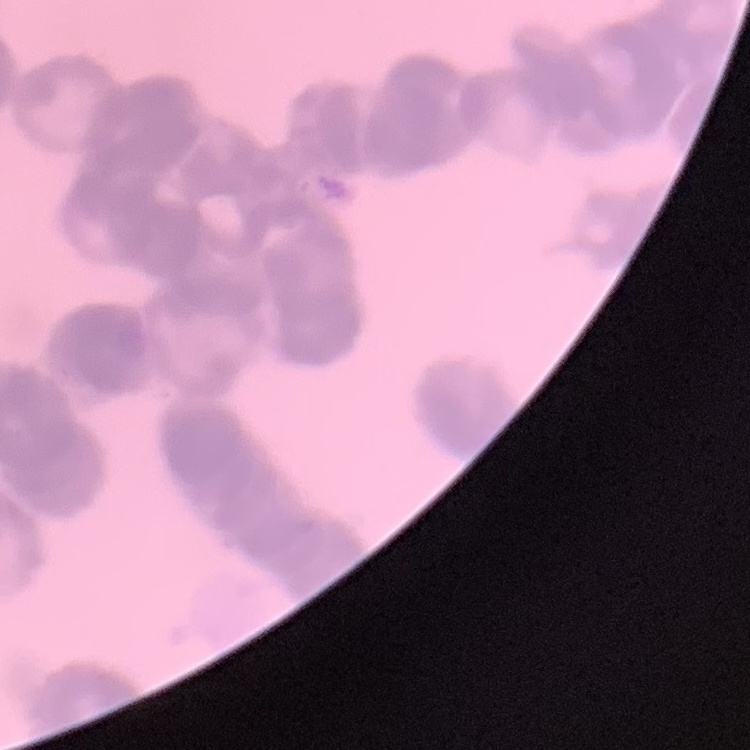

red_blood_cell_morphology: rouleaux formation
stain: Field's or Giemsa
preparation: thin peripheral smear
image_type: square crop of a larger photomicrograph